Report the malaria status of this cell.
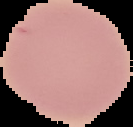

Uninfected.

Summary:
  - Preparation: thin blood film
  - Image type: segmented cell region on a black background
  - Image size: 133×127 pixels